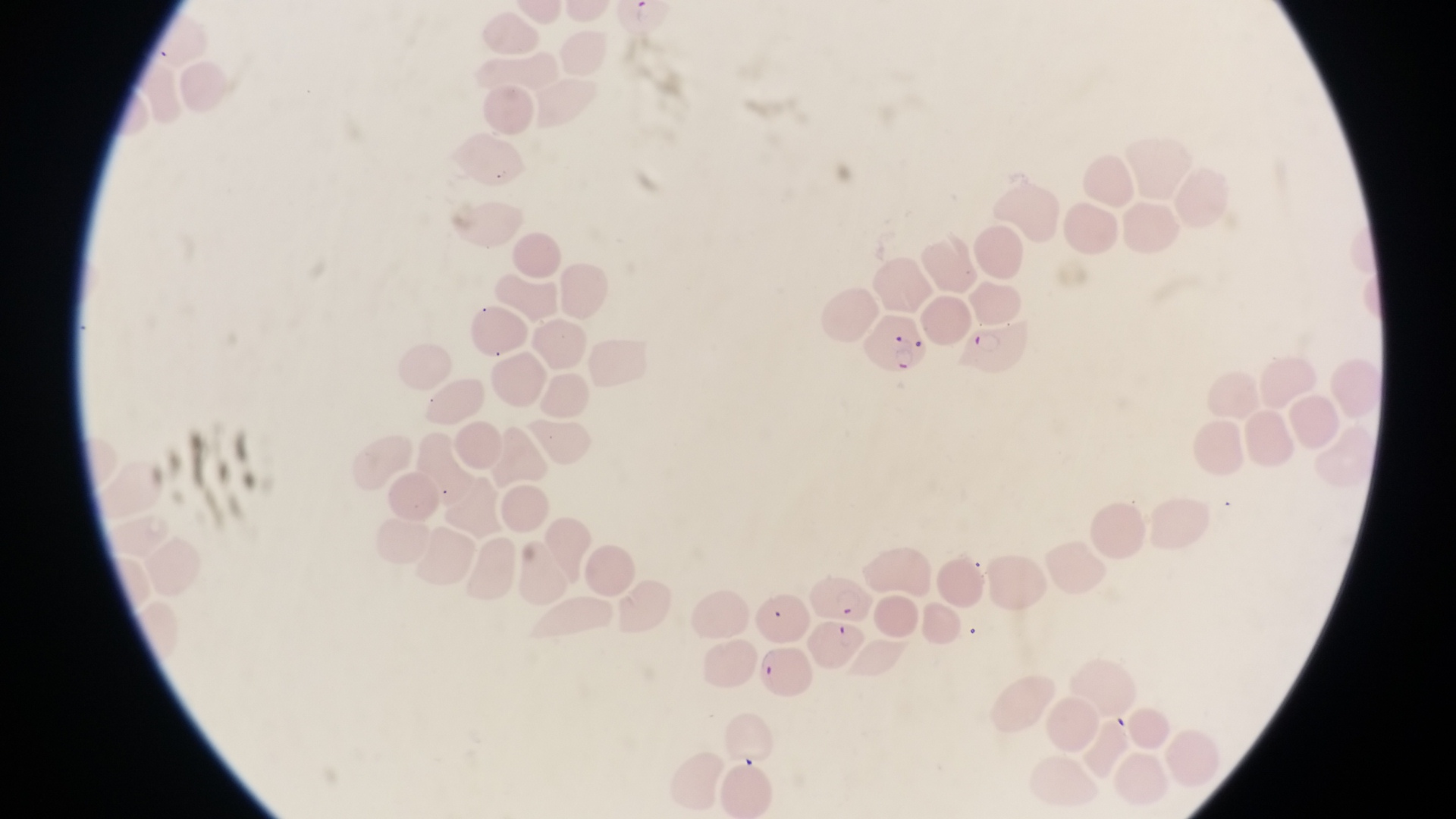

Approximate bounding boxes as left top right bottom in pixels.
Summary:
  - Parasitised red blood cell locations: 864 314 933 374; 965 323 1041 383; 808 565 868 620; 812 616 865 672; 761 645 816 698
  - Field of view: single
  - Image size: 1456×819 pixels
  - Preparation: thin blood film
  - Capture: smartphone photograph through the eyepiece of an Olympus CX-23 microscope
  - Country: Uganda
  - Magnification: 1000x